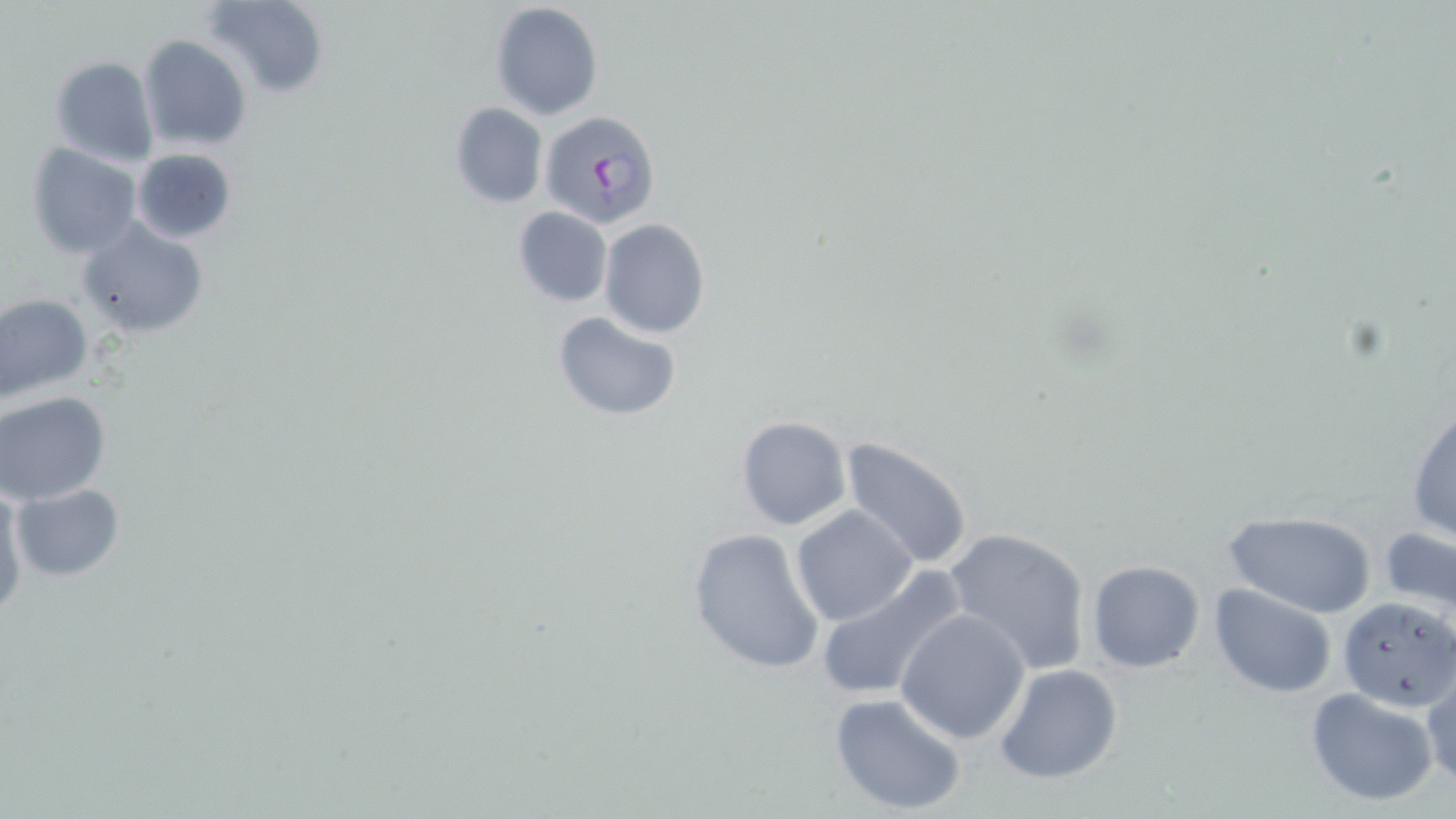

Summary:
  - Coordinate format: approximate bounding boxes as named x1/y1/x2/y2 corners in pixels
  - Uninfected red blood cell locations: (x1=205, y1=0, x2=330, y2=97), (x1=488, y1=1, x2=604, y2=121), (x1=139, y1=35, x2=252, y2=154), (x1=49, y1=55, x2=159, y2=167), (x1=448, y1=102, x2=547, y2=209), (x1=25, y1=143, x2=142, y2=258), (x1=131, y1=148, x2=238, y2=245), (x1=512, y1=206, x2=613, y2=308), (x1=76, y1=217, x2=208, y2=339), (x1=597, y1=218, x2=711, y2=339), (x1=0, y1=292, x2=93, y2=406), (x1=552, y1=311, x2=683, y2=422), (x1=0, y1=390, x2=111, y2=503), (x1=1407, y1=405, x2=1456, y2=545), (x1=734, y1=415, x2=851, y2=531), (x1=838, y1=437, x2=976, y2=572), (x1=11, y1=482, x2=125, y2=580), (x1=0, y1=486, x2=27, y2=613), (x1=792, y1=506, x2=919, y2=626), (x1=1224, y1=510, x2=1376, y2=618), (x1=942, y1=525, x2=1093, y2=675), (x1=1378, y1=526, x2=1456, y2=619), (x1=686, y1=527, x2=825, y2=675), (x1=1086, y1=560, x2=1207, y2=673), (x1=814, y1=566, x2=968, y2=704), (x1=1208, y1=584, x2=1338, y2=699), (x1=1338, y1=596, x2=1454, y2=711), (x1=897, y1=607, x2=1031, y2=743), (x1=993, y1=664, x2=1125, y2=785), (x1=1423, y1=676, x2=1455, y2=786), (x1=1305, y1=687, x2=1438, y2=806), (x1=828, y1=692, x2=967, y2=817)
  - Plasmodium falciparum-infected red blood cell locations: (x1=540, y1=109, x2=660, y2=229)
  - Slide-level diagnosis: Plasmodium falciparum
  - Preparation: thin blood smear
  - Image size: 1456×819 pixels
  - Stain: May-Grünwald-Giemsa
  - Modality: optical microscopy
  - Field of view: single
  - Magnification: 1000x